State which parasite is depicted.
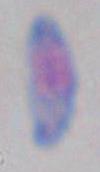
Toxoplasma gondii.

modality = photomicrograph
magnification = 1000x